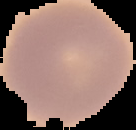

From a thin blood smear. Result: no malaria parasites detected. Cell region segmented out of the field of view; the surrounding area is masked to black. Image is 136×130 pixels.